Assess for Plasmodium parasites.
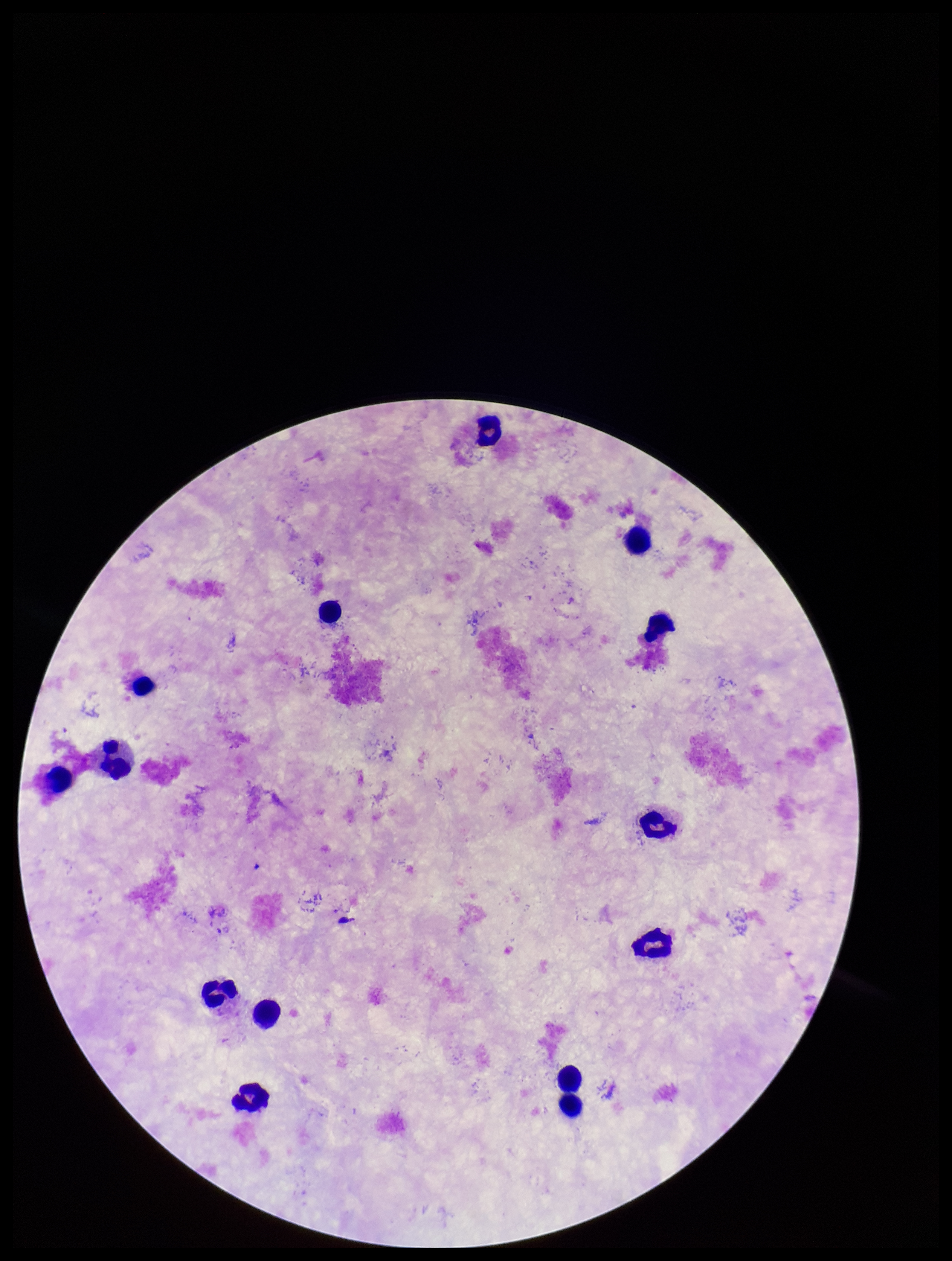
None seen.

stain = Giemsa
patient malaria status = negative
field of view = single
parasite count = 0
preparation = thick smear
leukocyte count = 14
image size = 952×1261 pixels
capture = smartphone photograph through the microscope eyepiece